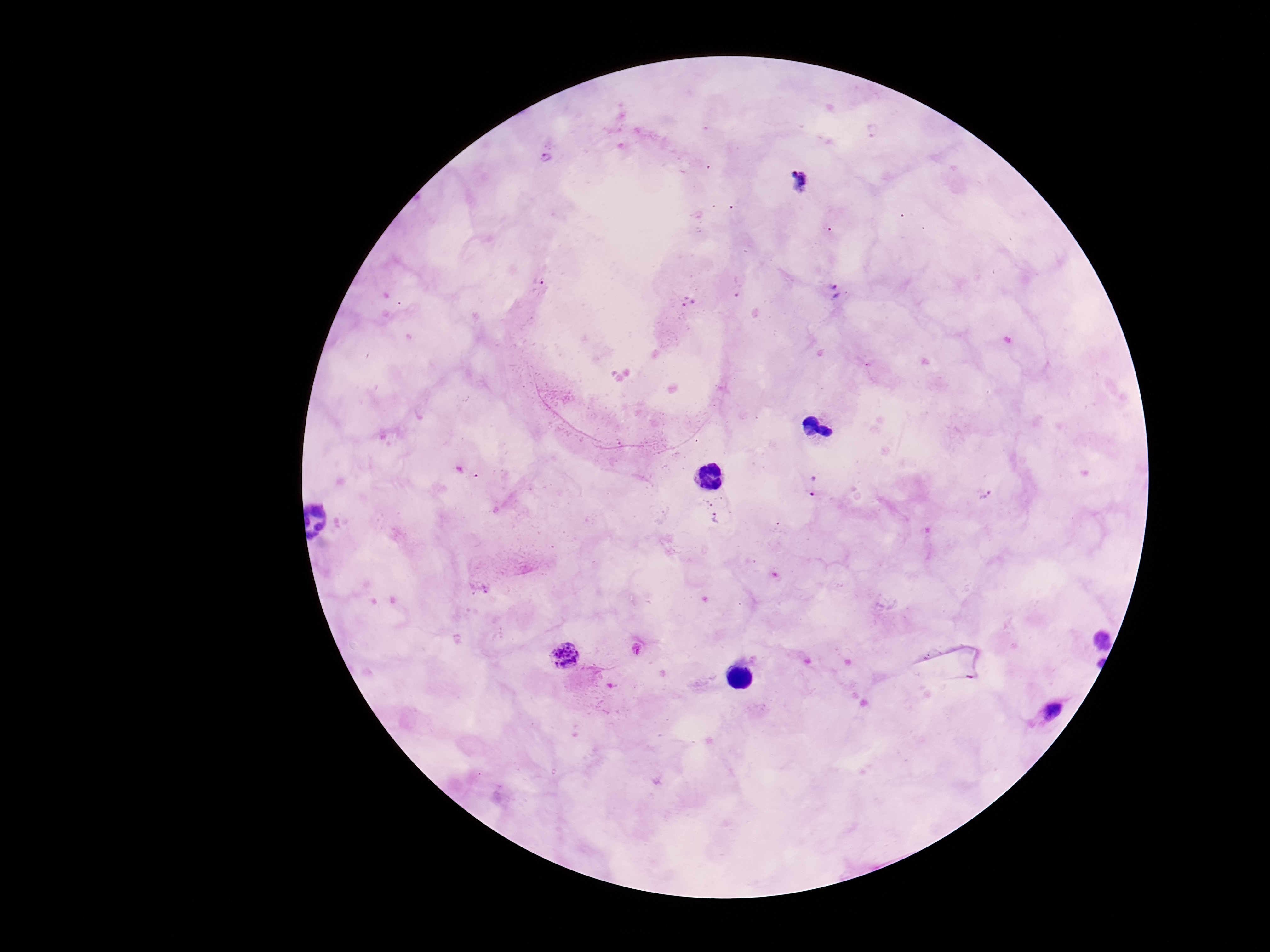 Approximate centers as {x, y} in pixels. Plasmodium parasite locations: {546, 157}, {539, 279}, {833, 293}, {688, 303}, {816, 487}, {984, 493}, {707, 501}, {718, 519}, {638, 649}, {566, 656}, {1052, 711}. Giemsa-stained preparation. Patient malaria status: infected. Image is 1270×952 pixels. One field from this slide. Thick blood film. Photographed through the microscope eyepiece with a smartphone camera. 100x magnification.